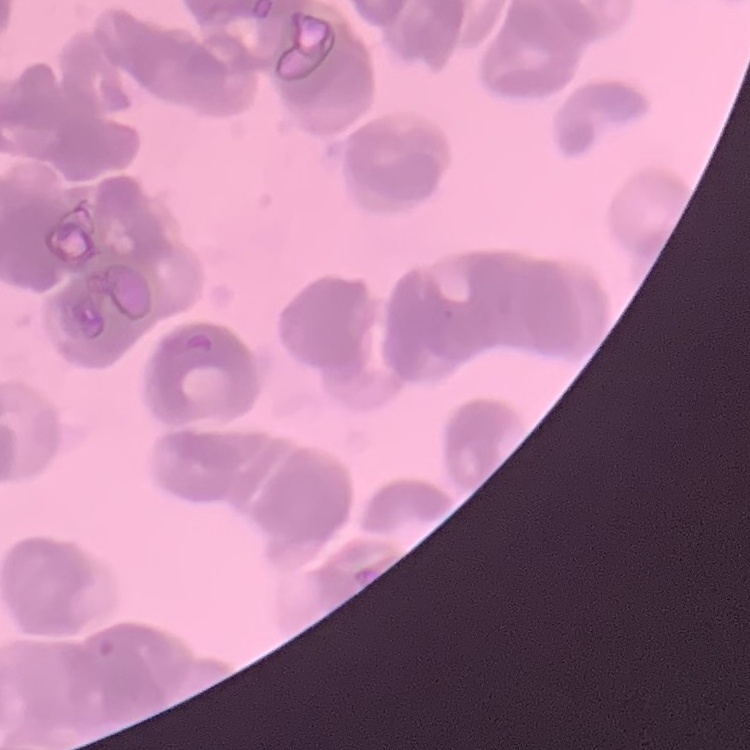
erythrocyte_morphology: rouleaux formation
image_type: one tile cut from a larger photomicrograph
stain: Field's or Giemsa
preparation: thin blood smear